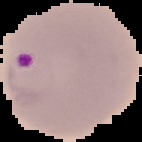

preparation = thin blood smear
image size = 142×142 pixels
image type = segmented cell region on a black background
result = Plasmodium parasites identified